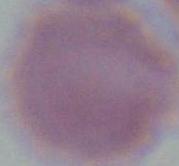
magnification = 1000x
identification = red blood cell
modality = photomicrograph